Locate every Babesia divergens-infected red blood cell.
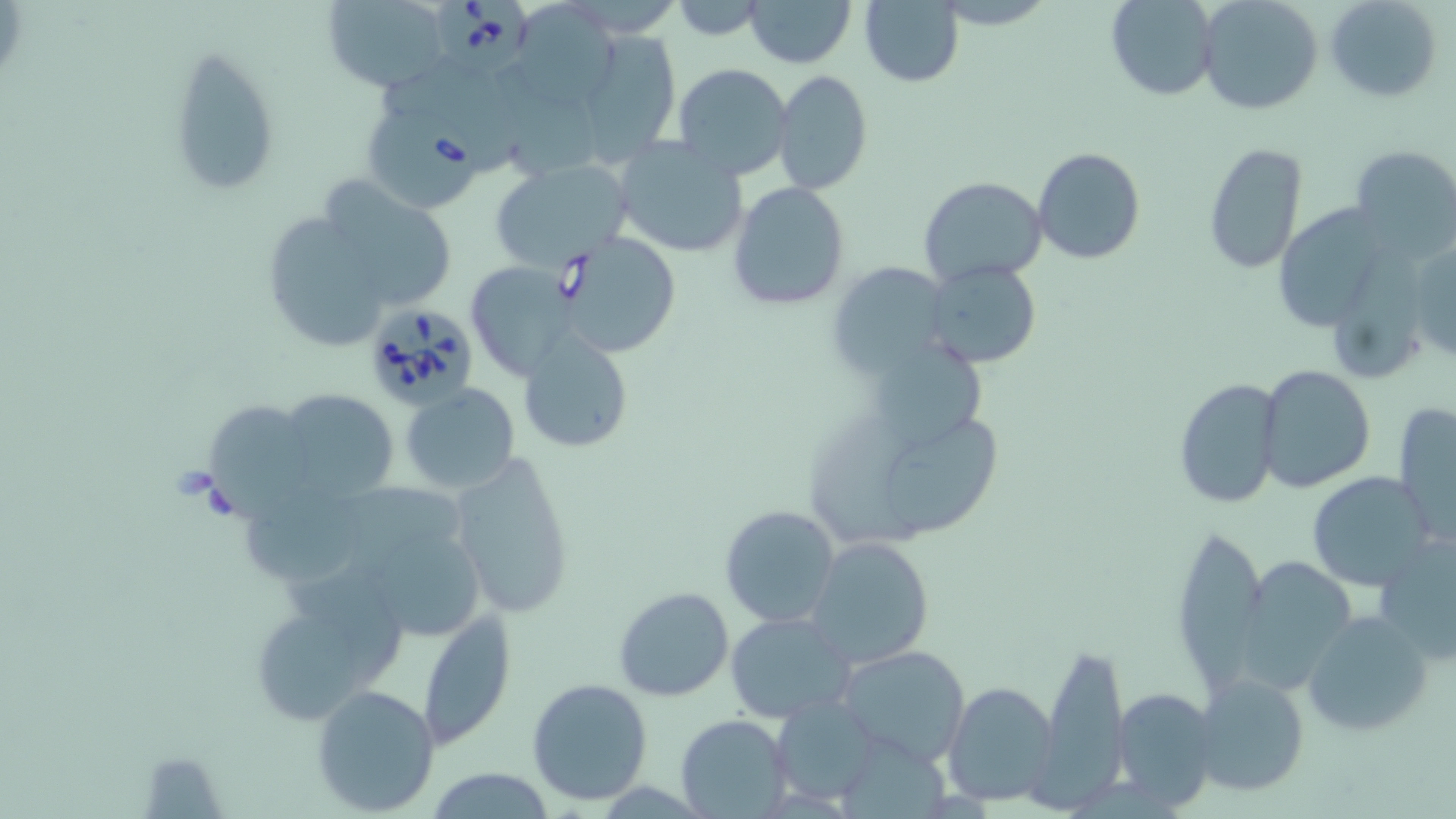

Approximate bounding boxes as (x1, y1, x2, y2) in pixels.
Babesia divergens-infected red blood cells: (437, 0, 536, 81), (366, 104, 486, 212), (554, 231, 683, 358), (360, 298, 481, 412).

Summary:
  - Uninfected red blood cell locations: (743, 0, 855, 68), (861, 0, 965, 87), (1325, 0, 1442, 101), (321, 1, 453, 95), (669, 1, 769, 39), (1105, 1, 1218, 100), (1198, 1, 1321, 115), (519, 9, 631, 114), (587, 31, 679, 163), (167, 46, 280, 196), (674, 63, 793, 180), (772, 71, 873, 196), (612, 136, 749, 260), (1202, 140, 1308, 277), (1349, 146, 1456, 262), (1032, 147, 1145, 263), (490, 162, 633, 273), (918, 176, 1050, 289), (727, 182, 853, 310), (282, 184, 461, 334), (1282, 196, 1390, 330), (1410, 235, 1455, 366), (826, 258, 956, 382), (922, 260, 1043, 370), (468, 265, 578, 371), (515, 329, 634, 454), (1258, 365, 1377, 494), (1173, 375, 1285, 513), (400, 383, 521, 494), (276, 389, 401, 500), (808, 389, 1008, 551), (206, 400, 311, 522), (1393, 402, 1456, 545), (447, 450, 578, 622), (1306, 470, 1436, 592), (249, 484, 361, 593), (719, 504, 842, 629), (1177, 532, 1263, 691), (380, 533, 492, 637), (805, 536, 934, 669), (1375, 536, 1456, 666), (1245, 554, 1364, 694), (613, 585, 735, 703), (416, 610, 515, 749), (1301, 610, 1435, 739), (725, 612, 855, 723), (261, 617, 363, 724), (1038, 638, 1130, 803), (837, 645, 970, 767), (1194, 672, 1310, 799), (527, 678, 654, 806), (944, 681, 1060, 806), (311, 684, 441, 814), (1110, 687, 1218, 811), (772, 692, 883, 805), (676, 712, 792, 817), (422, 767, 558, 818)
  - Slide-level diagnosis: Babesia divergens
  - Preparation: thin blood smear
  - Magnification: 1000x
  - Stain: May-Grünwald-Giemsa
  - Image size: 1456×819 pixels
  - Modality: optical microscopy
  - Field of view: one of a larger specimen